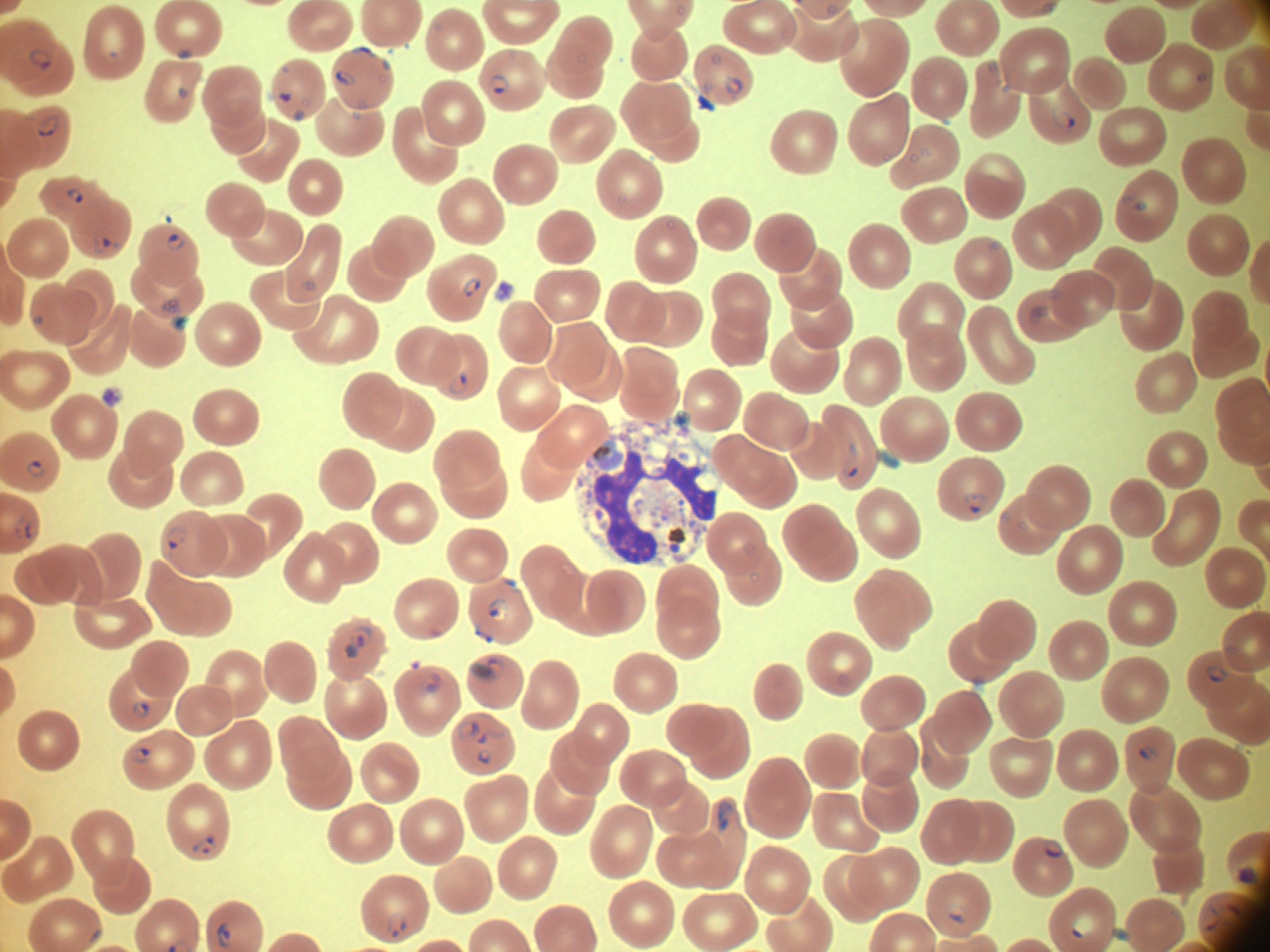

Approximate bounding boxes as named x1/y1/x2/y2 corners in pixels, from the source annotation, which is not necessarily exhaustive. Ring form locations: (x1=1045, y1=2, x2=1057, y2=14), (x1=827, y1=3, x2=838, y2=14), (x1=675, y1=6, x2=686, y2=16), (x1=29, y1=48, x2=52, y2=71), (x1=178, y1=48, x2=191, y2=59), (x1=352, y1=48, x2=375, y2=58), (x1=577, y1=53, x2=588, y2=65), (x1=711, y1=54, x2=722, y2=65), (x1=381, y1=60, x2=390, y2=70), (x1=988, y1=61, x2=998, y2=72), (x1=335, y1=70, x2=356, y2=85), (x1=1196, y1=72, x2=1207, y2=83), (x1=489, y1=74, x2=509, y2=93), (x1=723, y1=75, x2=744, y2=94), (x1=1003, y1=85, x2=1009, y2=93), (x1=177, y1=87, x2=187, y2=98), (x1=278, y1=93, x2=291, y2=102), (x1=302, y1=98, x2=310, y2=107), (x1=1051, y1=108, x2=1075, y2=132), (x1=293, y1=111, x2=304, y2=121), (x1=351, y1=112, x2=360, y2=119), (x1=38, y1=115, x2=61, y2=137), (x1=920, y1=148, x2=929, y2=157), (x1=883, y1=153, x2=891, y2=161), (x1=910, y1=153, x2=919, y2=162), (x1=67, y1=187, x2=83, y2=204), (x1=617, y1=194, x2=627, y2=204), (x1=1134, y1=201, x2=1147, y2=211), (x1=666, y1=221, x2=675, y2=229), (x1=168, y1=234, x2=185, y2=250), (x1=93, y1=235, x2=110, y2=253), (x1=463, y1=278, x2=481, y2=296), (x1=304, y1=281, x2=316, y2=290), (x1=1047, y1=289, x2=1061, y2=298), (x1=162, y1=298, x2=182, y2=315), (x1=1030, y1=306, x2=1048, y2=323), (x1=34, y1=316, x2=44, y2=324), (x1=449, y1=375, x2=467, y2=394), (x1=843, y1=442, x2=858, y2=478), (x1=27, y1=460, x2=45, y2=477), (x1=963, y1=493, x2=986, y2=513), (x1=15, y1=519, x2=31, y2=540), (x1=166, y1=526, x2=186, y2=550), (x1=749, y1=572, x2=759, y2=583), (x1=487, y1=597, x2=509, y2=620), (x1=346, y1=624, x2=374, y2=658), (x1=487, y1=658, x2=505, y2=677), (x1=471, y1=662, x2=488, y2=677), (x1=1205, y1=666, x2=1228, y2=682), (x1=424, y1=673, x2=440, y2=690), (x1=836, y1=673, x2=850, y2=687), (x1=132, y1=701, x2=150, y2=718), (x1=458, y1=721, x2=478, y2=739), (x1=472, y1=731, x2=488, y2=743), (x1=1140, y1=746, x2=1157, y2=760), (x1=132, y1=747, x2=151, y2=763), (x1=477, y1=749, x2=491, y2=763), (x1=717, y1=802, x2=733, y2=831), (x1=192, y1=835, x2=216, y2=855), (x1=1044, y1=839, x2=1063, y2=857), (x1=1237, y1=867, x2=1256, y2=884), (x1=946, y1=904, x2=967, y2=923), (x1=1202, y1=906, x2=1220, y2=931), (x1=387, y1=912, x2=405, y2=938), (x1=1072, y1=916, x2=1093, y2=937), (x1=217, y1=922, x2=232, y2=947). Ring forms too small for a box (approximate object centers, named x/y in pixels): (x=285, y=69). Image is 1270×952 pixels. Single field of view. Giemsa-stained preparation. Thin blood film. Species: Plasmodium falciparum. Acquired with a Leica DM2000 optical microscope and its built-in camera. Captured at 100x magnification.